Locate and identify every blood parasite.
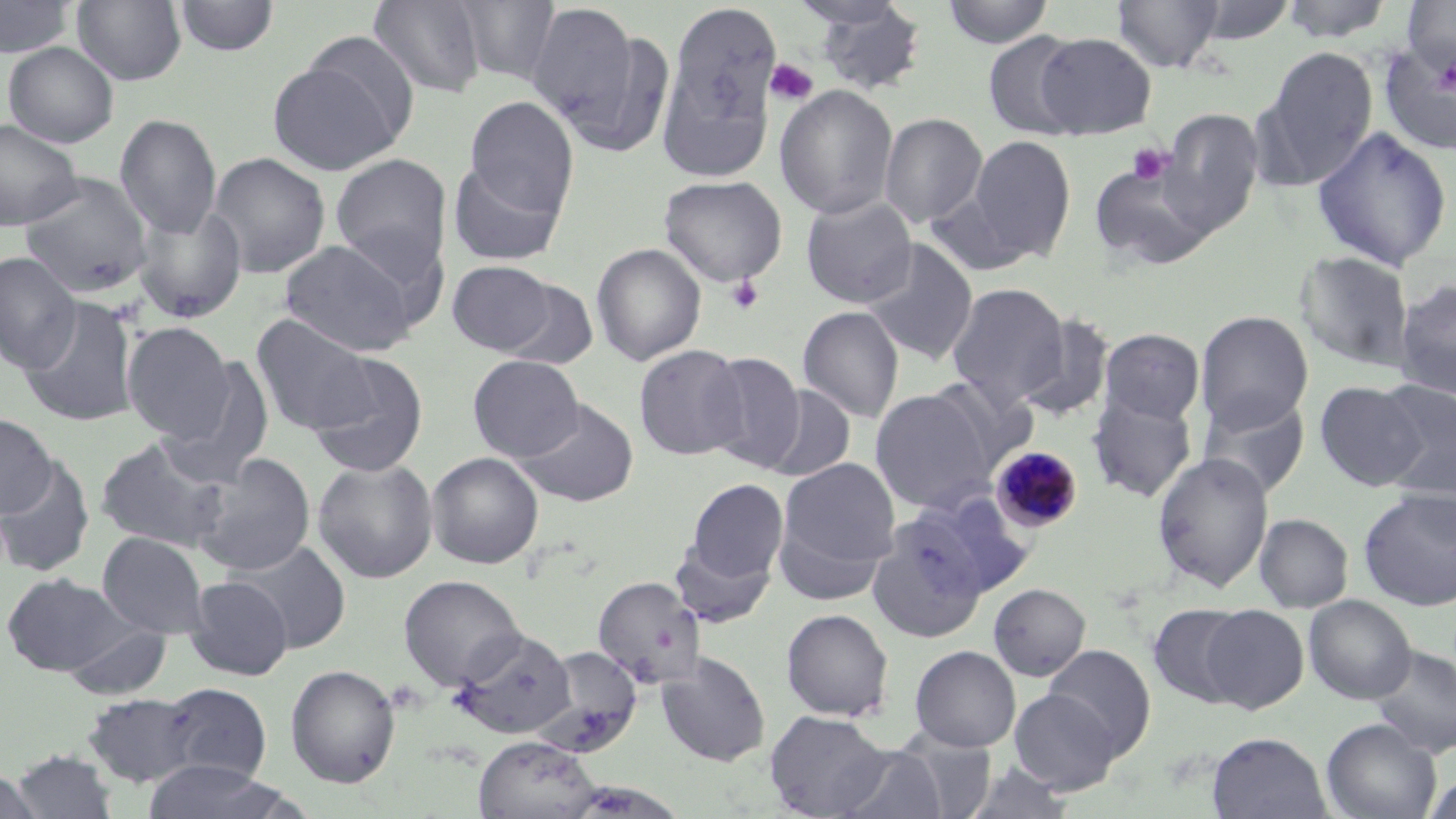

Approximate bounding boxes as [x1, y1, x2, y2] in pixels.
Plasmodium malariae-infected red blood cells: [990, 446, 1084, 534].
No Plasmodium falciparum, Plasmodium ovale, Plasmodium vivax, Babesia divergens, or Trypanosoma brucei observed.

{
  "slide_level_diagnosis": "Plasmodium malariae",
  "preparation": "thin blood film",
  "magnification": "1000x",
  "uninfected_red_blood_cell_locations": "approximate bounding boxes as [x1, y1, x2, y2] in pixels: [0, 0, 76, 59], [72, 0, 186, 86], [174, 0, 280, 57], [367, 0, 486, 98], [454, 0, 561, 85], [667, 0, 782, 142], [940, 0, 1055, 48], [1111, 0, 1227, 73], [1187, 0, 1298, 45], [1278, 0, 1395, 43], [805, 1, 928, 98], [1403, 1, 1456, 75], [524, 3, 643, 133], [560, 25, 676, 157], [983, 32, 1086, 141], [1034, 32, 1157, 139], [3, 42, 119, 147], [1380, 43, 1456, 155], [1260, 46, 1378, 187], [267, 54, 407, 175], [775, 84, 897, 220], [465, 97, 579, 218], [1158, 108, 1264, 234], [878, 113, 987, 228], [115, 114, 222, 238], [0, 118, 84, 232], [1311, 125, 1453, 271], [967, 135, 1076, 261], [207, 152, 330, 278], [330, 153, 452, 278], [1087, 158, 1217, 270], [448, 159, 566, 266], [19, 172, 153, 298], [659, 175, 787, 288], [800, 194, 918, 308], [133, 203, 248, 324], [278, 239, 420, 356], [862, 240, 978, 365], [591, 242, 707, 366], [1296, 251, 1415, 372], [1, 252, 82, 374], [447, 260, 556, 355], [1393, 278, 1456, 398], [498, 279, 599, 371], [947, 283, 1070, 408], [19, 296, 140, 427], [798, 306, 904, 423], [1195, 311, 1313, 432], [1015, 313, 1115, 422], [251, 314, 375, 435], [121, 322, 235, 441], [1100, 328, 1205, 424], [633, 344, 748, 461], [701, 352, 807, 472], [306, 353, 430, 478], [467, 355, 585, 462], [163, 357, 276, 484], [923, 375, 1038, 477], [1315, 381, 1427, 490], [1375, 381, 1456, 499], [760, 385, 856, 483], [869, 388, 995, 513], [1087, 390, 1197, 503], [1198, 393, 1311, 498], [515, 398, 639, 507], [0, 412, 56, 518], [95, 434, 235, 552], [426, 452, 544, 569], [1152, 452, 1274, 592], [190, 455, 316, 576], [0, 456, 95, 578], [312, 457, 439, 583], [779, 457, 901, 573], [686, 479, 788, 583], [1358, 488, 1456, 610], [914, 490, 1037, 599], [773, 511, 890, 606], [1254, 513, 1353, 613], [865, 515, 989, 642], [97, 531, 210, 639], [670, 539, 776, 627], [229, 540, 352, 652], [1, 572, 128, 676], [398, 574, 526, 691], [185, 575, 293, 680], [593, 576, 706, 688], [988, 583, 1091, 681], [1303, 595, 1416, 704], [1147, 603, 1253, 708], [1200, 604, 1309, 713], [781, 608, 894, 721], [64, 623, 171, 701], [450, 628, 576, 739], [1044, 644, 1156, 759], [1367, 644, 1456, 758], [909, 645, 1021, 751], [532, 646, 643, 758], [658, 652, 771, 766], [286, 664, 401, 788], [159, 683, 272, 784], [1009, 688, 1121, 794], [82, 693, 199, 788], [764, 710, 891, 818], [1321, 718, 1442, 819], [892, 728, 997, 818], [1207, 732, 1331, 819], [474, 735, 600, 819], [836, 745, 948, 819], [10, 749, 118, 818], [141, 760, 294, 819], [957, 761, 1081, 818], [1, 767, 41, 819], [1422, 772, 1456, 819]",
  "platelet_locations": "approximate bounding boxes as [x1, y1, x2, y2] in pixels: [1434, 57, 1456, 96], [765, 58, 818, 106], [1127, 144, 1173, 186], [726, 275, 765, 314]",
  "stain": "May-Grünwald-Giemsa",
  "modality": "optical microscopy",
  "field_of_view": "one of a larger specimen",
  "image_size": "1456×819 pixels"
}